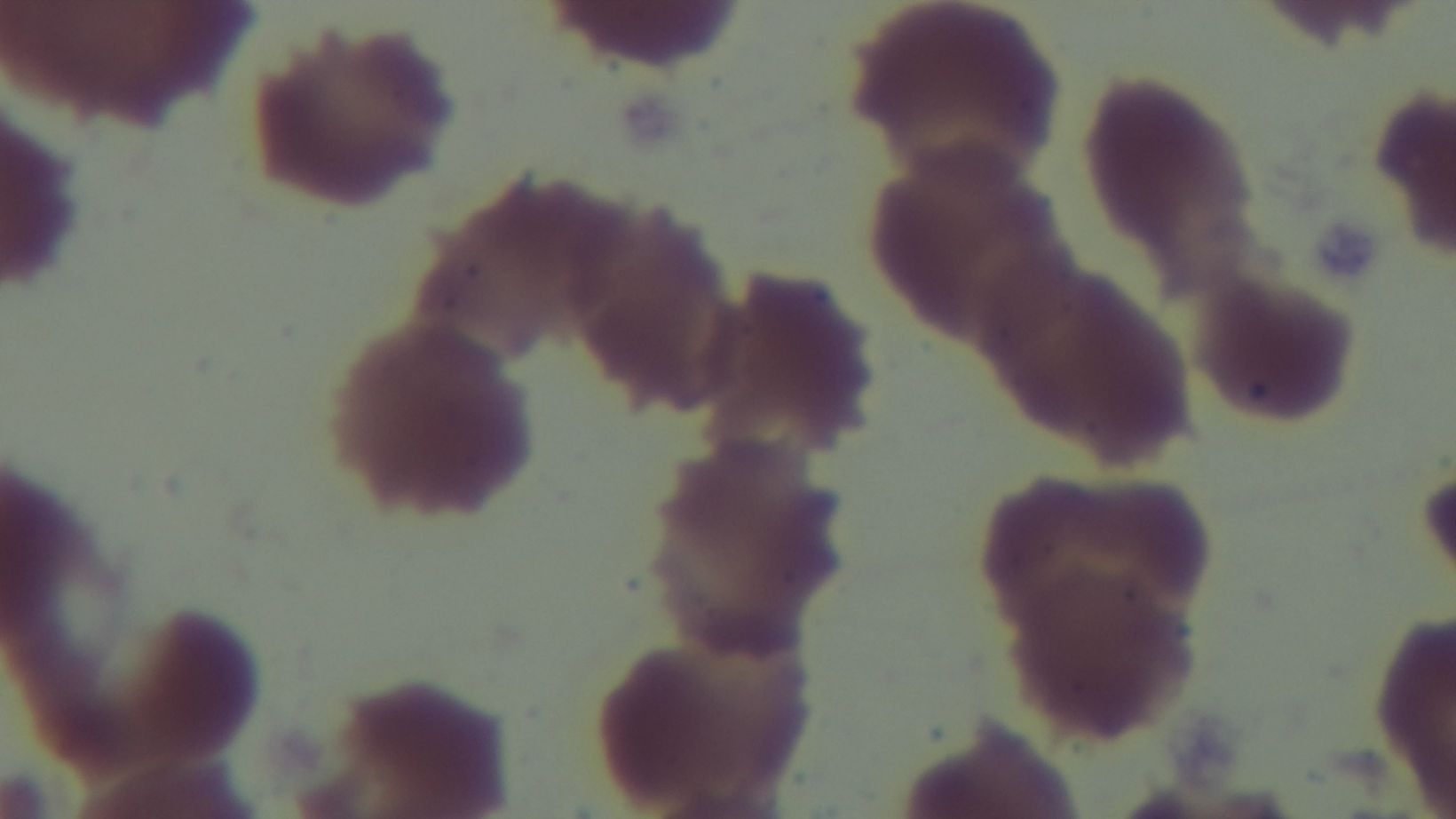
stain = Giemsa
malaria status = uninfected
modality = light microscopy
capture = mounted 4K digital camera
field of view = one from the slide
preparation = thin
objective = 100x oil immersion